State which parasite is depicted.
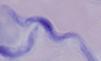
A trypanosome.

Summary:
  - Modality: photomicrograph
  - Magnification: 1000x